Name the blood parasite species.
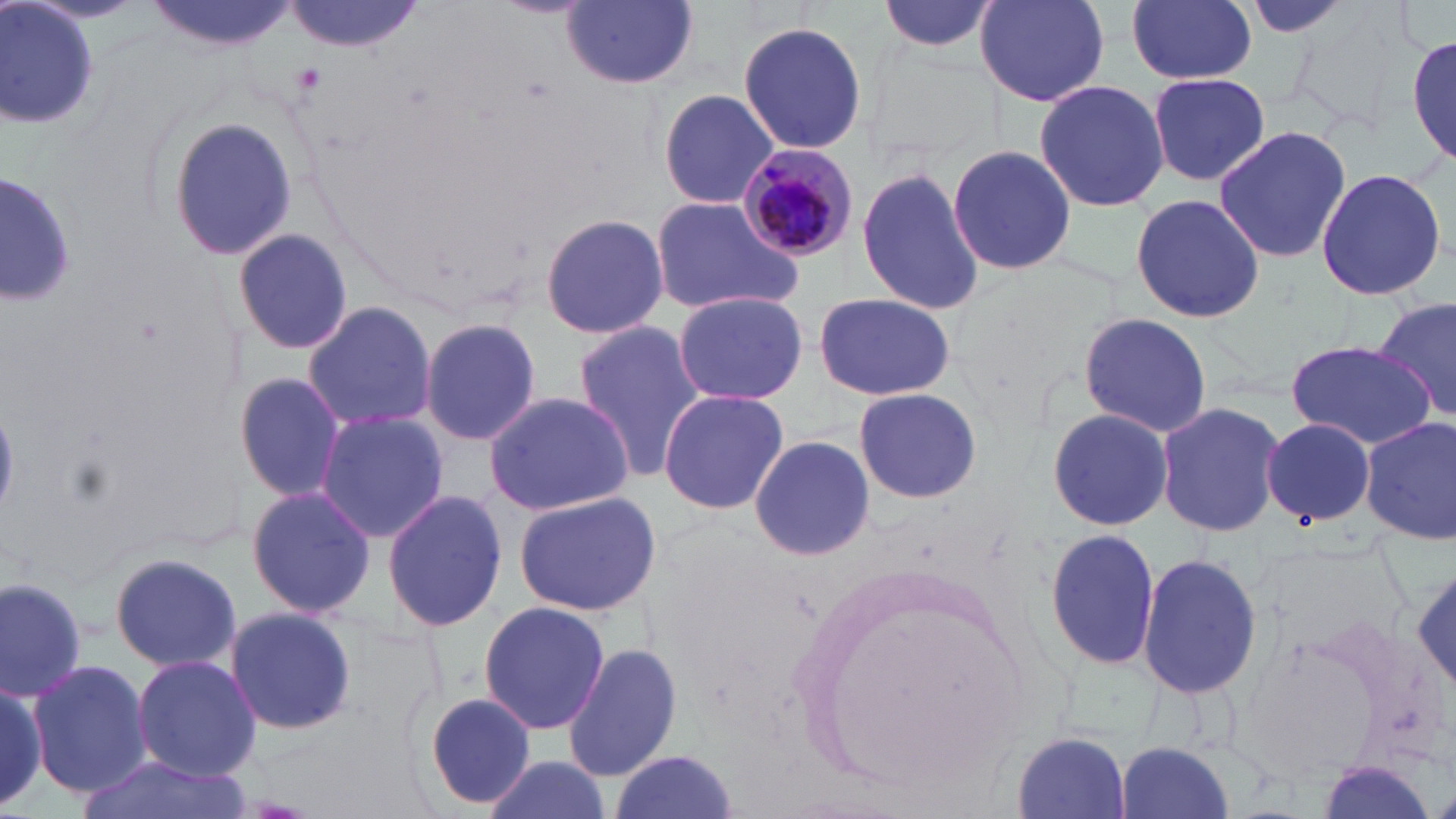

Plasmodium malariae.

magnification: 1000x
field_of_view: single
image_size: 1456×819 pixels
modality: light microscopy
preparation: thin blood film
stain: May-Grünwald-Giemsa
uninfected_red_blood_cell_locations: 'approximate bounding boxes as [x1, y1, x2, y2] in pixels: [142, 0, 303, 52], [287, 0, 425, 56], [876, 0, 1001, 57], [973, 0, 1110, 105], [1127, 0, 1256, 85], [1237, 0, 1357, 40], [1289, 0, 1423, 137], [2, 1, 100, 133], [561, 1, 698, 89], [736, 20, 868, 156], [1407, 25, 1456, 169], [1145, 72, 1273, 189], [1032, 79, 1171, 212], [657, 88, 778, 209], [167, 116, 298, 261], [1212, 124, 1353, 264], [944, 143, 1077, 277], [855, 163, 987, 319], [1314, 166, 1450, 303], [0, 172, 80, 307], [1129, 193, 1265, 323], [650, 197, 805, 316], [538, 212, 668, 340], [232, 227, 353, 358], [672, 290, 808, 406], [812, 292, 955, 402], [1373, 295, 1455, 422], [302, 301, 438, 430], [1077, 311, 1212, 437], [420, 315, 544, 449], [572, 321, 706, 481], [1286, 338, 1434, 449], [233, 371, 347, 504], [853, 386, 983, 504], [657, 387, 790, 516], [482, 390, 634, 515], [1156, 399, 1285, 539], [1046, 407, 1175, 532], [315, 410, 447, 541], [1261, 417, 1377, 529], [1360, 418, 1456, 546], [747, 433, 875, 563], [246, 486, 377, 620], [382, 489, 509, 631], [511, 491, 663, 616], [1044, 527, 1164, 670], [107, 551, 243, 674], [1138, 552, 1263, 703], [1409, 564, 1456, 697], [0, 575, 90, 701], [478, 603, 611, 736], [224, 607, 357, 736], [563, 644, 681, 784], [133, 655, 261, 780], [27, 660, 153, 798], [0, 674, 52, 812], [419, 691, 537, 812], [1010, 732, 1134, 818], [1111, 739, 1238, 819], [608, 751, 737, 819], [79, 752, 240, 819], [481, 753, 608, 819], [1310, 758, 1441, 819]'
plasmodium_malariae_infected_red_blood_cell_locations: 'approximate bounding boxes as [x1, y1, x2, y2] in pixels: [734, 142, 856, 263]'